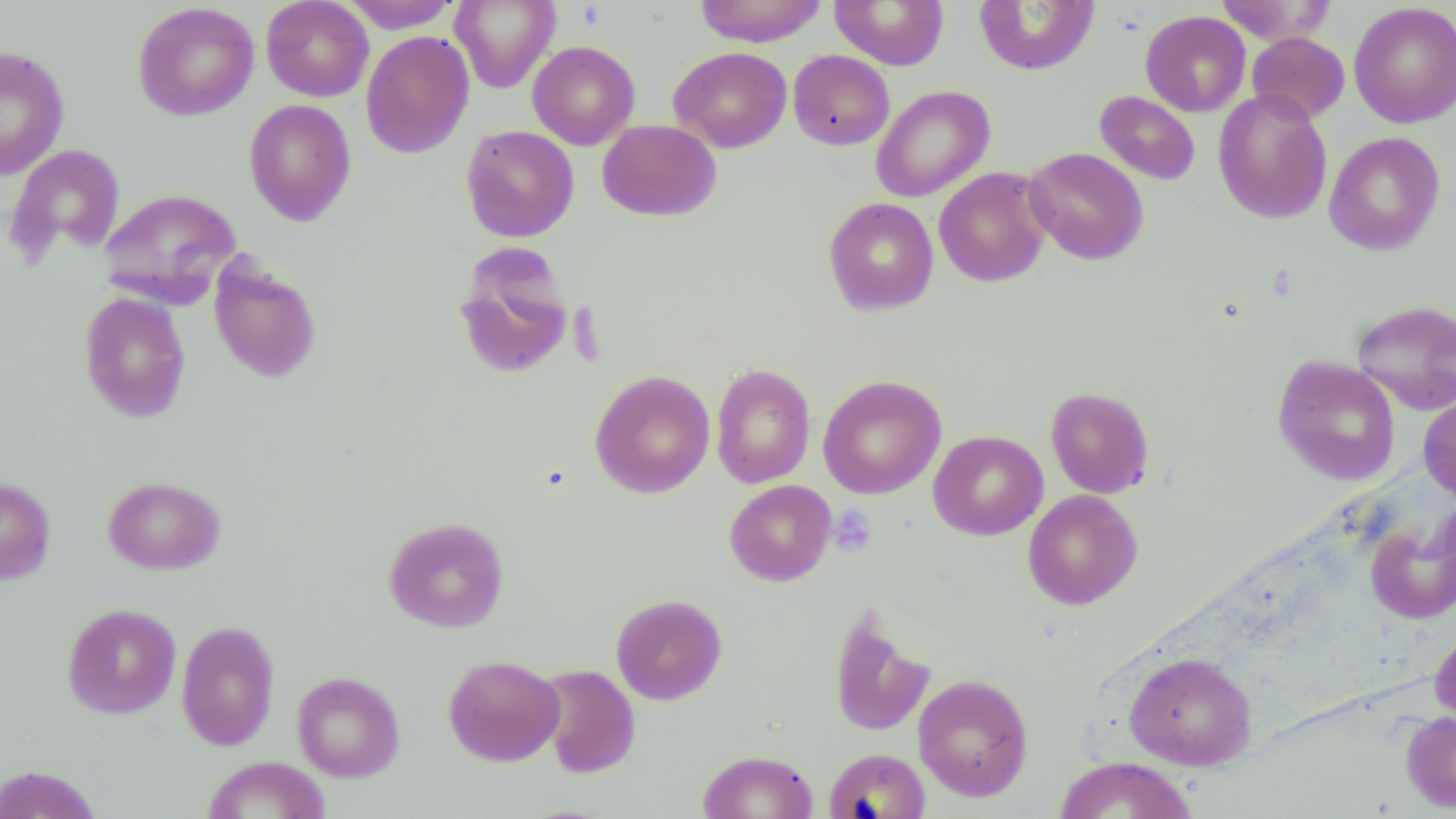

Summary:
  - Coordinate format: approximate bounding boxes as [x1, y1, x2, y2] in pixels
  - Uninfected red blood cell locations: [261, 0, 374, 101], [694, 0, 827, 47], [1215, 0, 1337, 45], [341, 1, 461, 33], [449, 1, 560, 93], [830, 1, 949, 70], [974, 1, 1099, 74], [131, 2, 260, 121], [1349, 2, 1456, 128], [1140, 11, 1251, 116], [360, 30, 474, 159], [1247, 32, 1350, 124], [527, 41, 640, 150], [0, 46, 70, 180], [669, 46, 792, 152], [788, 50, 895, 150], [871, 85, 995, 202], [1213, 89, 1332, 224], [1094, 91, 1201, 185], [243, 99, 357, 227], [597, 119, 721, 222], [461, 125, 579, 242], [1324, 131, 1445, 255], [7, 144, 126, 262], [1024, 147, 1148, 265], [934, 167, 1053, 287], [99, 188, 241, 304], [823, 197, 939, 316], [450, 245, 579, 382], [208, 258, 322, 383], [78, 291, 192, 423], [1351, 299, 1456, 414], [1273, 355, 1401, 485], [710, 364, 816, 488], [589, 369, 716, 498], [817, 375, 946, 499], [1045, 386, 1155, 498], [1418, 392, 1456, 506], [928, 430, 1048, 541], [102, 475, 225, 574], [0, 476, 56, 585], [724, 480, 836, 586], [1022, 489, 1142, 610], [1366, 512, 1456, 624], [383, 516, 510, 633], [610, 593, 728, 705], [62, 603, 181, 719], [827, 604, 936, 738], [176, 619, 280, 752], [1430, 622, 1456, 724], [1123, 652, 1257, 769], [443, 655, 565, 766], [537, 664, 641, 778], [291, 670, 405, 782], [913, 674, 1034, 801], [1401, 710, 1456, 813], [824, 747, 931, 819], [698, 749, 818, 819], [201, 756, 331, 819], [1053, 756, 1197, 818], [0, 764, 103, 819]
  - Platelet locations: [828, 505, 878, 556]
  - Slide-level diagnosis: negative for blood parasites
  - Preparation: thin blood film
  - Modality: light microscopy
  - Magnification: 1000x
  - Field of view: single
  - Image size: 1456×819 pixels
  - Stain: May-Grünwald-Giemsa